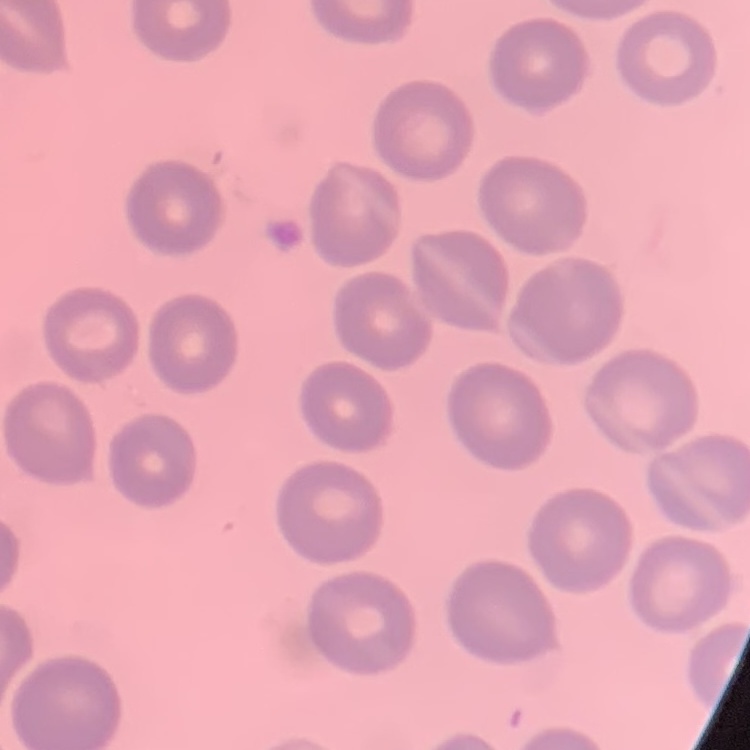
{
  "red_blood_cell_morphology": "no rouleaux formation",
  "stain": "Field's or Giemsa",
  "preparation": "thin peripheral smear",
  "image_type": "square crop of a larger photomicrograph"
}